Assess for malaria.
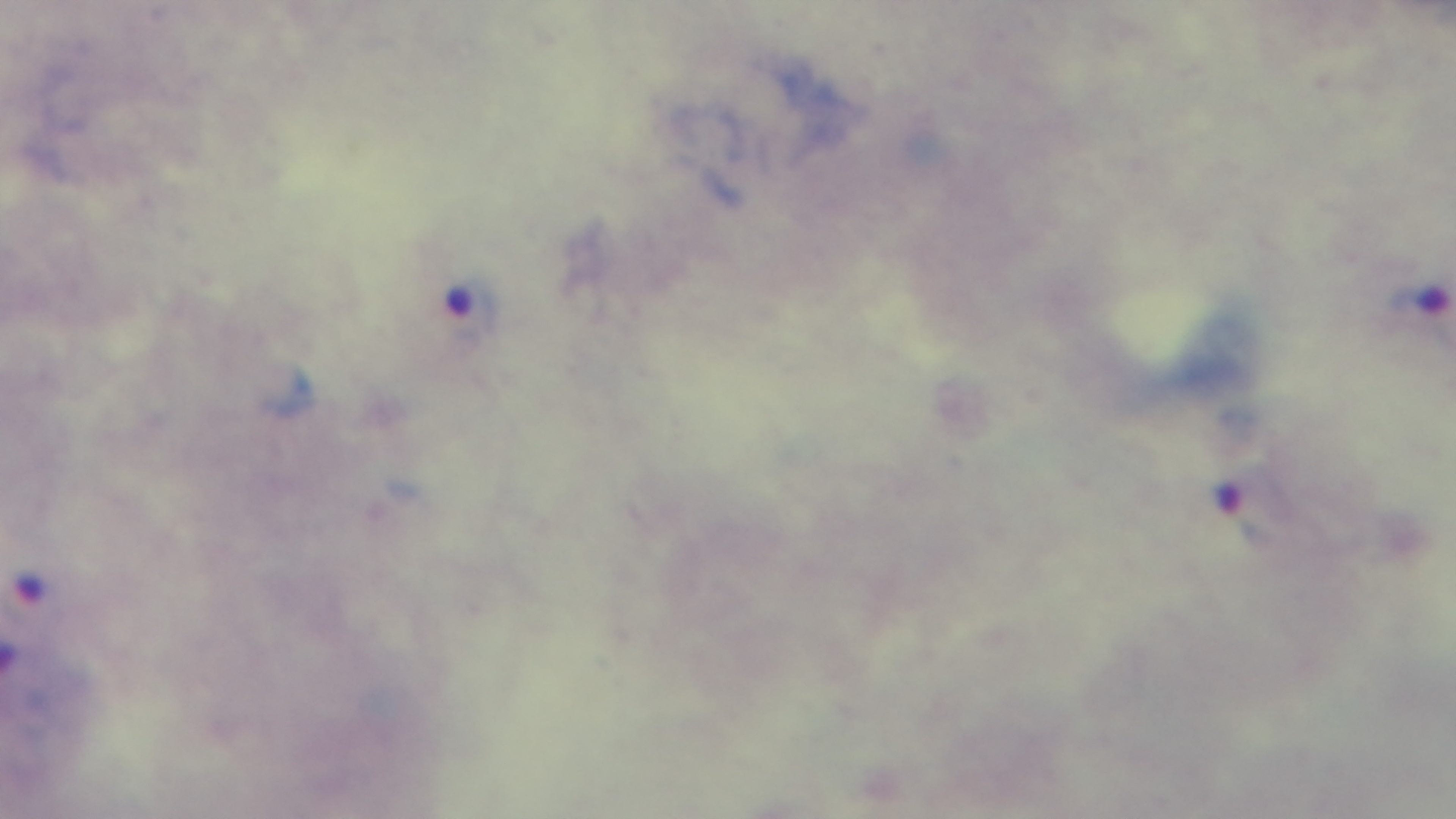
It is infected.

100x oil-immersion objective. Single field of view. Captured with a mounted 4K digital camera. Giemsa-stained. Preparation: thick smear. Light microscopy.